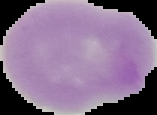
result: no Plasmodium parasites seen
preparation: thin blood smear
image_size: 157×115 pixels
image_type: segmented cell region with the area outside set to black